Outline each blood parasite and name the species.
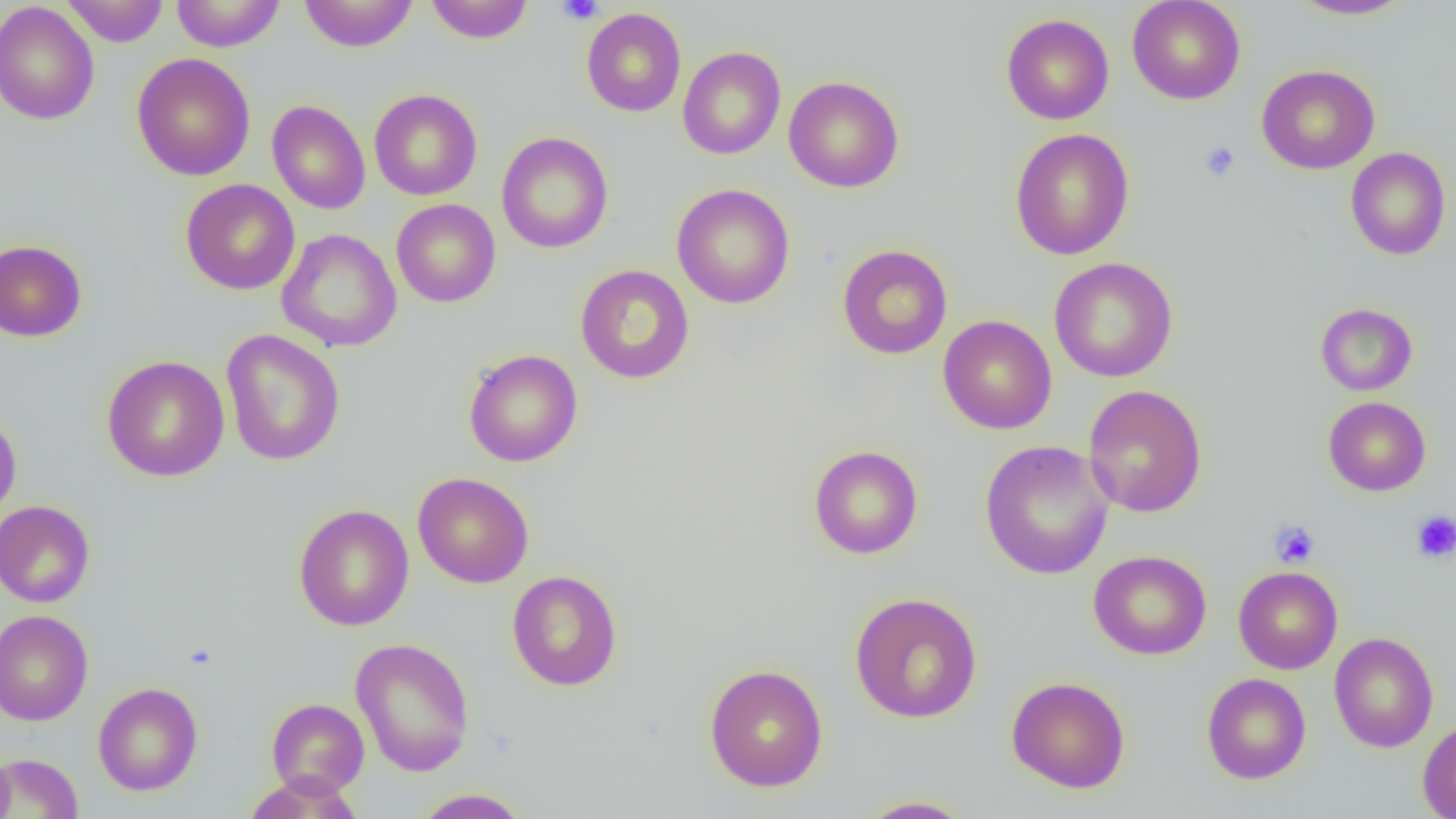
No blood parasites seen.

Summary:
  - Coordinate format: approximate bounding boxes as (x1, y1, x2, y2) in pixels
  - Uninfected red blood cell locations: (62, 0, 169, 46), (171, 0, 286, 52), (299, 0, 418, 52), (425, 0, 534, 43), (1127, 0, 1246, 105), (1288, 0, 1414, 21), (0, 2, 100, 125), (581, 8, 686, 117), (1001, 13, 1114, 125), (677, 46, 786, 160), (132, 53, 256, 181), (1257, 64, 1380, 174), (784, 76, 904, 193), (369, 89, 482, 200), (267, 99, 371, 214), (1010, 128, 1134, 260), (496, 131, 613, 253), (1345, 147, 1451, 261), (180, 178, 300, 295), (671, 183, 795, 309), (391, 199, 501, 307), (276, 229, 402, 352), (0, 239, 87, 342), (837, 244, 952, 360), (1049, 257, 1178, 382), (575, 264, 695, 384), (1315, 303, 1417, 396), (937, 315, 1057, 434), (221, 329, 345, 466), (464, 349, 583, 467), (102, 354, 230, 482), (1083, 385, 1207, 518), (1323, 396, 1431, 496), (0, 411, 22, 524), (979, 440, 1114, 580), (808, 444, 923, 559), (412, 472, 534, 588), (0, 500, 95, 608), (294, 503, 414, 631), (1088, 550, 1212, 660), (1233, 566, 1342, 674), (506, 570, 622, 691), (849, 592, 982, 723), (0, 609, 94, 725), (1329, 631, 1439, 752), (350, 637, 475, 776), (704, 663, 828, 793), (1202, 673, 1311, 784), (1006, 676, 1131, 793), (92, 682, 203, 796), (266, 698, 370, 797), (1417, 718, 1456, 819), (0, 748, 16, 818), (0, 752, 84, 818), (412, 788, 531, 818), (854, 795, 978, 818)
  - Platelet locations: (557, 0, 603, 24), (1199, 141, 1240, 182), (1411, 511, 1456, 563), (1269, 520, 1319, 568)
  - Slide-level diagnosis: negative for blood parasites
  - Image size: 1456×819 pixels
  - Preparation: thin blood film
  - Modality: light microscopy
  - Field of view: one of a larger specimen
  - Magnification: 1000x